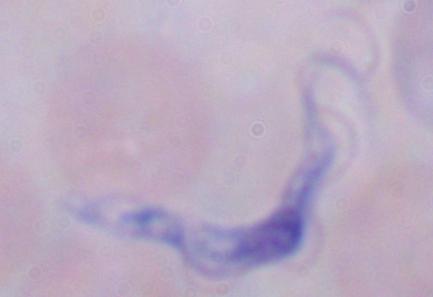

Photomicrograph. Captured at 1000x magnification. A trypanosome is seen.